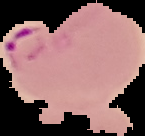

Cell region segmented out of the field of view; the surrounding area is masked to black. From a thin blood smear. Malaria status: parasitized. Image is 145×136 pixels.